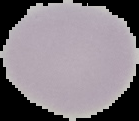 The area outside the segmented cell region is set to black. Image is 139×121 pixels. Result: no Plasmodium parasites detected. From a thin blood film.